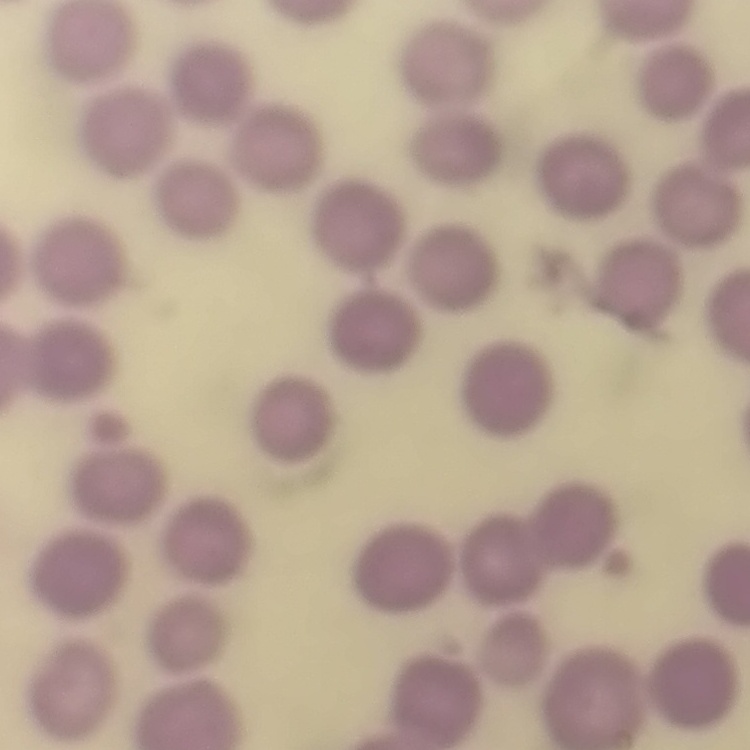
The red blood cells show no rouleaux formation. Field's or Giemsa stain. Thin peripheral smear. Square crop of a larger photomicrograph.